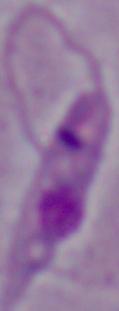

magnification = 1000x
modality = photomicrograph
identification = Leishmania